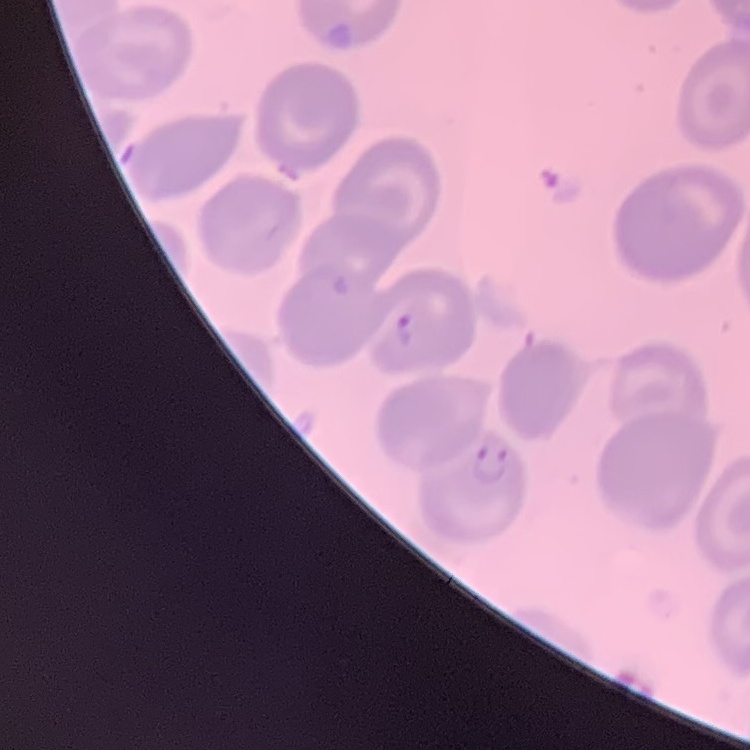

Summary:
  - Red blood cell morphology: no rouleaux formation
  - Stain: Field's or Giemsa
  - Image type: one tile cut from a larger photomicrograph
  - Preparation: thin blood smear